Give the position of every Plasmodium falciparum parasite, noting its life-cycle stage.
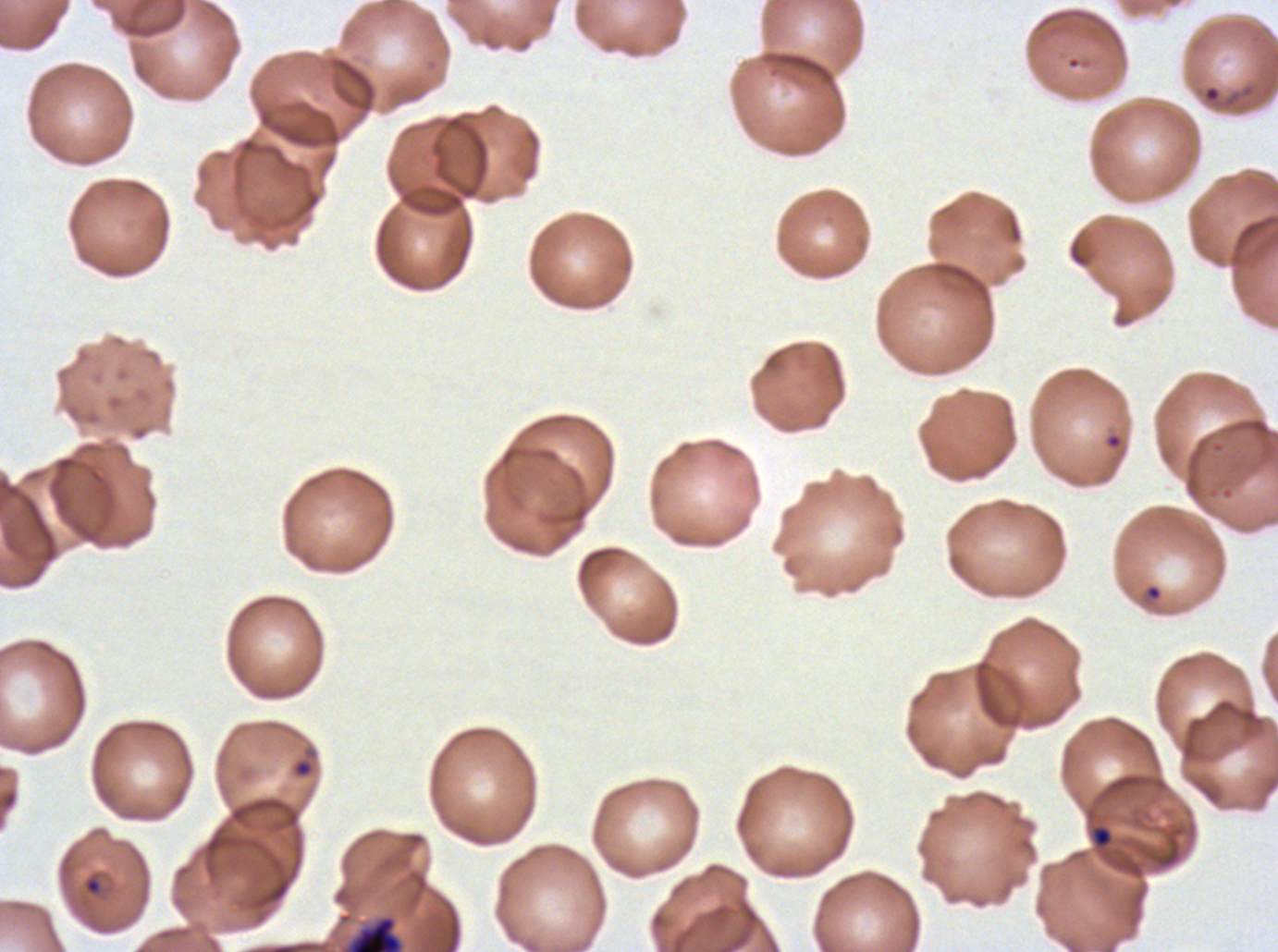

Approximate bounding boxes as {x1, y1, x2, y2} in pixels.
Rings: {1202, 84, 1222, 104}, {1144, 583, 1163, 602}, {290, 746, 318, 780}, {1090, 824, 1113, 849}, {82, 874, 104, 897}.
Early schizonts: {350, 917, 401, 951}.
No late-ring/early-trophozoite forms, mid trophozoites, late trophozoites, late schizonts, segmenters, or gametocytes observed.

Thin blood smear. Giemsa stain. Life-cycle stages observed: ring, early schizont. Image is 1278×952 pixels. Ex-vivo Plasmodium falciparum culture from a patient in The Gambia, grown for 24 to 48 hours. One sub-image of a larger composite.